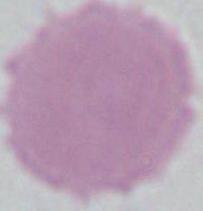
{
  "modality": "photomicrograph",
  "magnification": "1000x",
  "identification": "red blood cell"
}